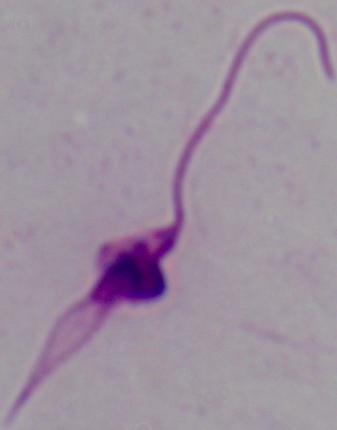
identification = Leishmania
magnification = 1000x
modality = micrograph